Identify the blood parasite species.
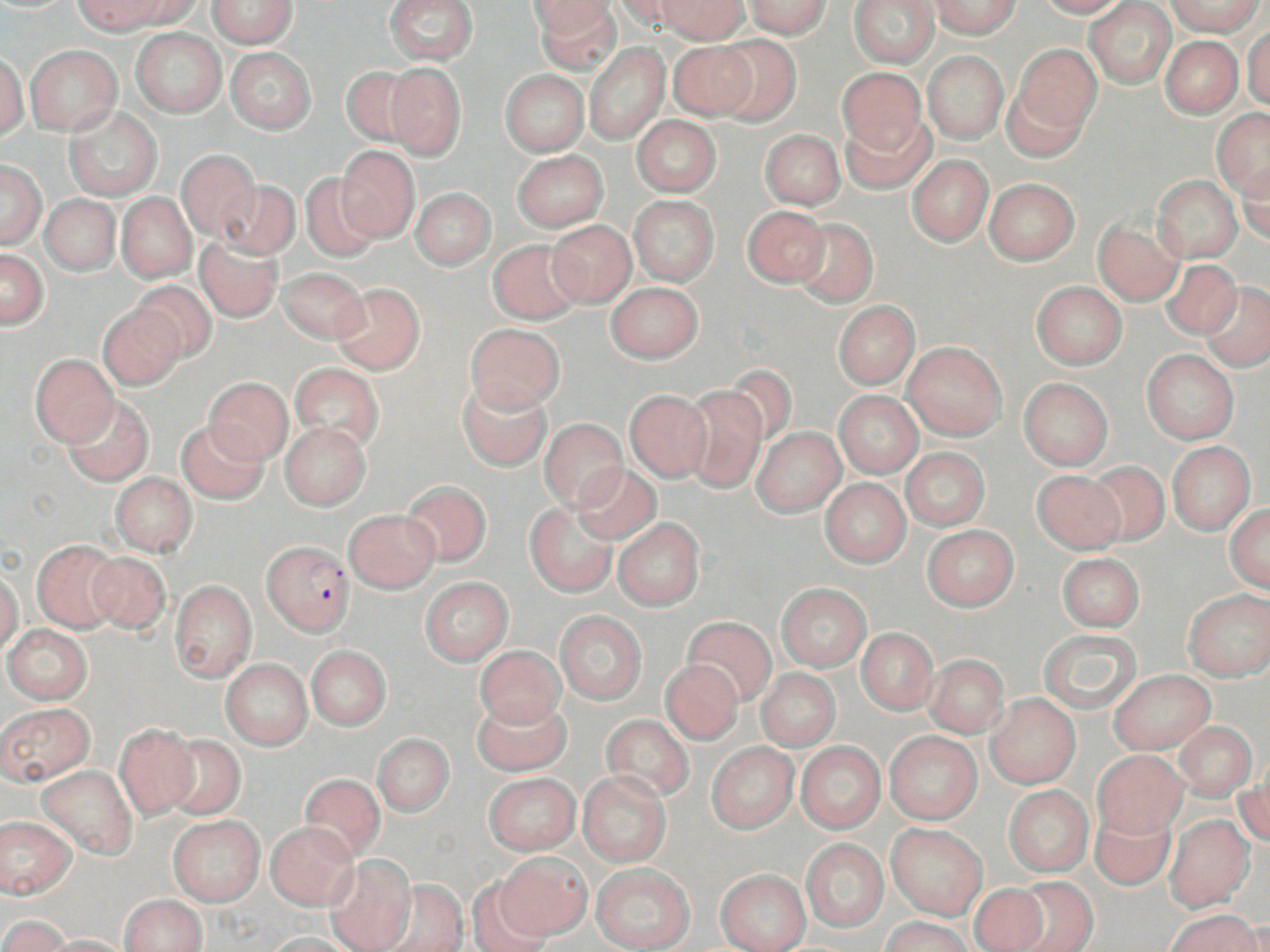
Plasmodium falciparum.

magnification: 1000x
stain: May-Grünwald-Giemsa
image_size: 1270×952 pixels
field_of_view: one of a larger specimen
uninfected_red_blood_cell_locations: 'approximate bounding boxes as (x1, y1, x2, y2) in pixels: (74, 0, 180, 35), (207, 0, 297, 48), (384, 0, 478, 65), (532, 0, 617, 71), (611, 0, 699, 35), (657, 0, 749, 43), (743, 0, 832, 37), (848, 0, 941, 67), (526, 1, 613, 34), (930, 1, 1020, 38), (1034, 1, 1131, 18), (1085, 2, 1176, 87), (1166, 2, 1266, 37), (1244, 23, 1270, 111), (131, 27, 226, 118), (713, 36, 800, 125), (1160, 36, 1244, 118), (668, 41, 760, 119), (585, 43, 669, 143), (25, 44, 121, 136), (1015, 44, 1101, 135), (225, 47, 316, 134), (1, 52, 27, 140), (923, 52, 1007, 142), (384, 63, 466, 161), (341, 66, 421, 145), (836, 67, 927, 152), (500, 70, 588, 156), (1002, 76, 1092, 161), (64, 106, 162, 201), (1211, 109, 1270, 198), (843, 114, 934, 193), (631, 116, 721, 196), (759, 129, 846, 209), (335, 145, 419, 242), (177, 150, 260, 240), (512, 151, 608, 230), (907, 155, 993, 246), (1237, 159, 1269, 244), (1, 162, 45, 248), (910, 166, 1077, 251), (300, 175, 382, 262), (1153, 175, 1242, 261), (983, 178, 1080, 264), (216, 179, 299, 260), (411, 187, 496, 269), (116, 193, 196, 282), (41, 194, 119, 276), (629, 196, 718, 286), (741, 205, 830, 288), (791, 216, 879, 308), (1093, 216, 1184, 306), (546, 220, 636, 306), (194, 236, 282, 322), (488, 239, 584, 325), (1, 250, 49, 329), (1161, 259, 1241, 339), (279, 268, 367, 344), (130, 280, 216, 362), (1031, 280, 1128, 370), (330, 282, 425, 374), (604, 282, 704, 362), (1199, 282, 1270, 371), (833, 301, 920, 389), (98, 304, 184, 392), (465, 324, 564, 412), (902, 341, 1008, 440), (1142, 350, 1239, 444), (31, 354, 118, 446), (290, 362, 385, 452), (720, 364, 797, 447), (205, 377, 293, 464), (1018, 378, 1113, 470), (458, 380, 552, 472), (680, 387, 768, 492), (834, 390, 924, 477), (624, 391, 712, 482), (61, 395, 152, 486), (539, 419, 627, 510), (177, 421, 269, 504), (279, 422, 370, 510), (753, 427, 845, 516), (1167, 441, 1255, 534), (901, 448, 991, 532), (1081, 460, 1171, 548), (570, 464, 661, 543), (1031, 469, 1125, 553), (110, 473, 198, 556), (820, 479, 911, 568), (401, 481, 491, 567), (525, 501, 618, 598), (1225, 502, 1270, 592), (344, 510, 439, 592), (612, 516, 706, 611), (922, 525, 1020, 611), (31, 539, 121, 633), (86, 551, 170, 634), (1056, 552, 1145, 632), (0, 571, 23, 655), (419, 577, 513, 664), (170, 579, 256, 681), (774, 582, 872, 671), (1183, 590, 1270, 679), (553, 610, 648, 704), (681, 617, 776, 706), (3, 625, 92, 704), (856, 627, 939, 714), (1037, 628, 1142, 713), (306, 645, 391, 730), (475, 645, 564, 728), (923, 654, 1009, 737), (221, 657, 312, 750), (660, 659, 742, 744), (756, 669, 840, 752), (1109, 670, 1216, 754), (985, 693, 1080, 788), (471, 696, 570, 775), (1, 702, 95, 785), (599, 715, 694, 801), (1172, 721, 1257, 800), (114, 722, 200, 819), (885, 731, 981, 824), (164, 734, 245, 820), (372, 735, 454, 816), (705, 741, 800, 834), (796, 741, 886, 833), (1093, 751, 1186, 838), (1235, 764, 1269, 850), (36, 765, 139, 859), (577, 771, 671, 867), (298, 772, 386, 860), (483, 773, 581, 855), (1002, 784, 1093, 877), (1089, 805, 1177, 891), (0, 816, 77, 898), (169, 816, 263, 905), (1163, 816, 1254, 912), (265, 821, 360, 910), (886, 824, 988, 920), (801, 838, 889, 931), (495, 852, 591, 940), (323, 853, 416, 952), (591, 864, 694, 951), (715, 868, 810, 952), (466, 877, 551, 952), (1006, 877, 1096, 952), (374, 880, 468, 952), (966, 883, 1051, 952), (118, 895, 207, 952), (1165, 908, 1264, 951), (1, 913, 71, 951), (879, 916, 975, 952), (264, 933, 359, 951), (43, 934, 130, 952)'
preparation: thin blood smear
modality: light microscopy
plasmodium_falciparum_infected_red_blood_cell_locations: 'approximate bounding boxes as (x1, y1, x2, y2) in pixels: (262, 541, 353, 635)'